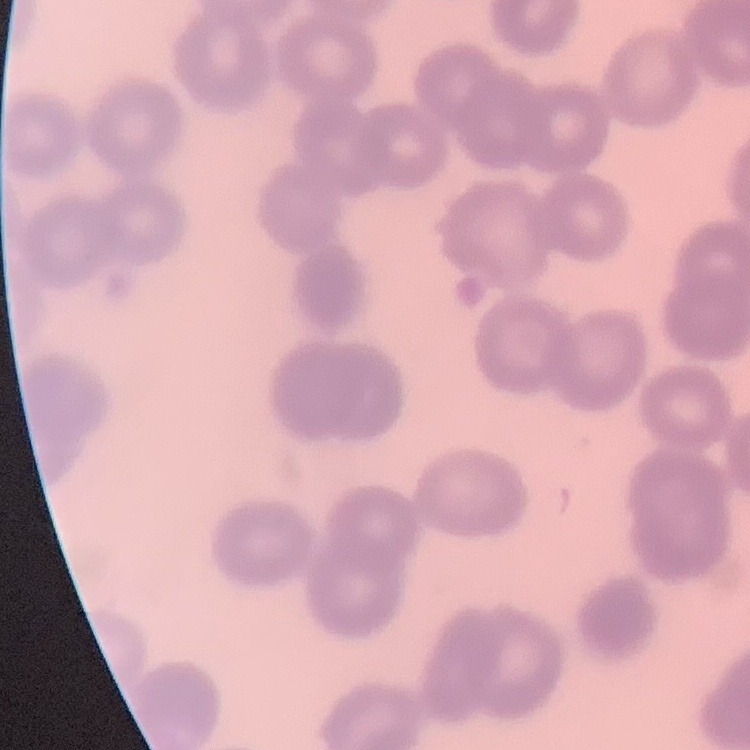

red_blood_cell_morphology: no rouleaux formation
stain: Field's or Giemsa
preparation: thin peripheral smear
image_type: square crop of a larger photomicrograph